Locate every Plasmodium parasite and every leukocyte.
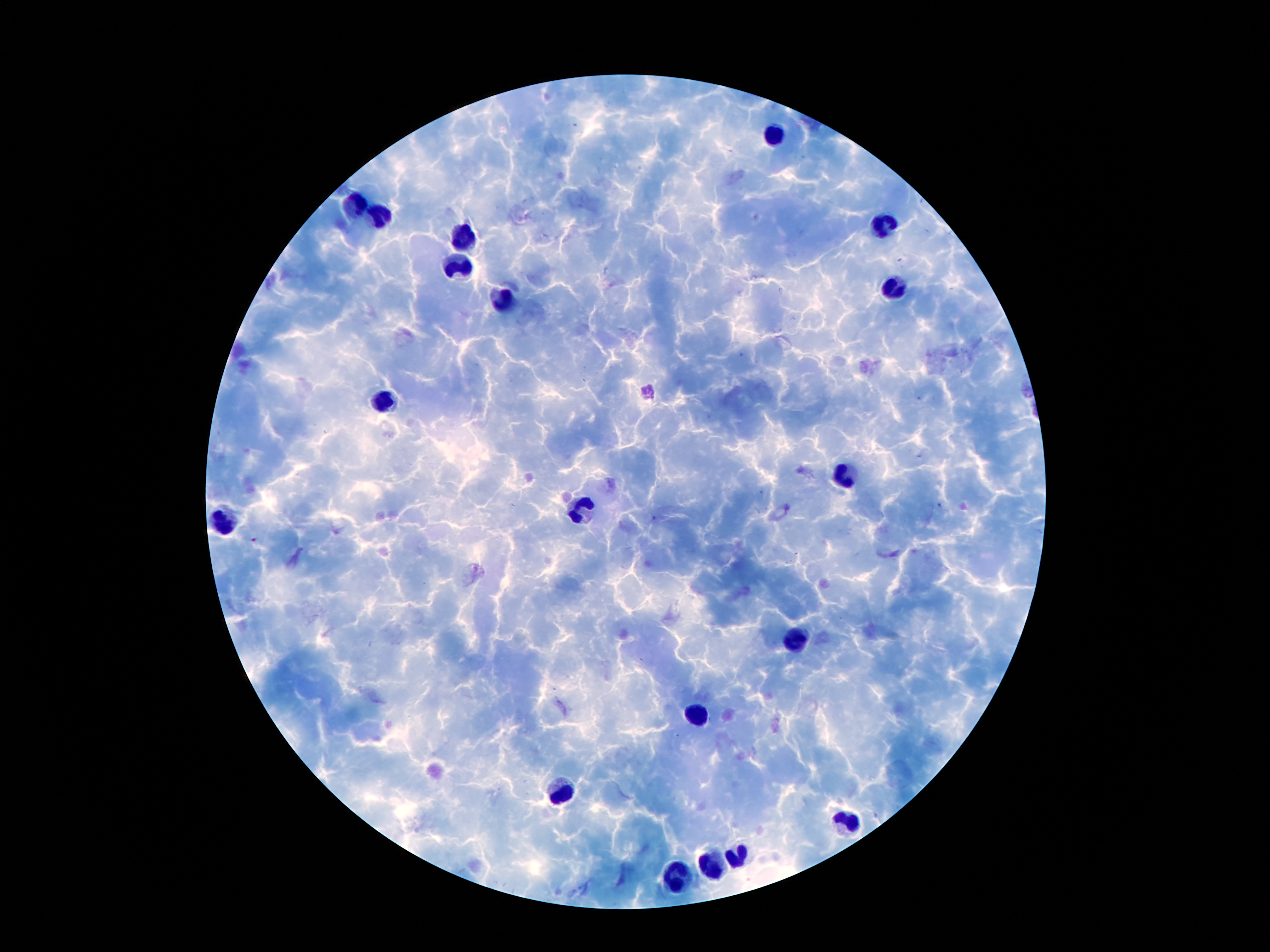
No Plasmodium parasites identified.
Approximate centers as {x, y} in pixels.
Leukocytes: {774, 135}, {359, 204}, {379, 217}, {880, 226}, {461, 240}, {458, 268}, {892, 291}, {509, 300}, {383, 402}, {843, 477}, {580, 510}, {223, 523}, {796, 639}, {698, 715}, {562, 796}, {848, 822}, {736, 855}, {713, 865}, {678, 881}.

Giemsa stain. Photographed through the microscope eyepiece with a smartphone camera. Patient malaria status: positive for Plasmodium falciparum. Image is 1270×952 pixels. Thick blood smear. Single field of view. 100x magnification.